Assess this cell for malaria.
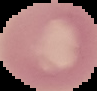
It is uninfected.

Summary:
  - Preparation: thin blood smear
  - Image type: segmented cell region with the area outside set to black
  - Image size: 97×91 pixels